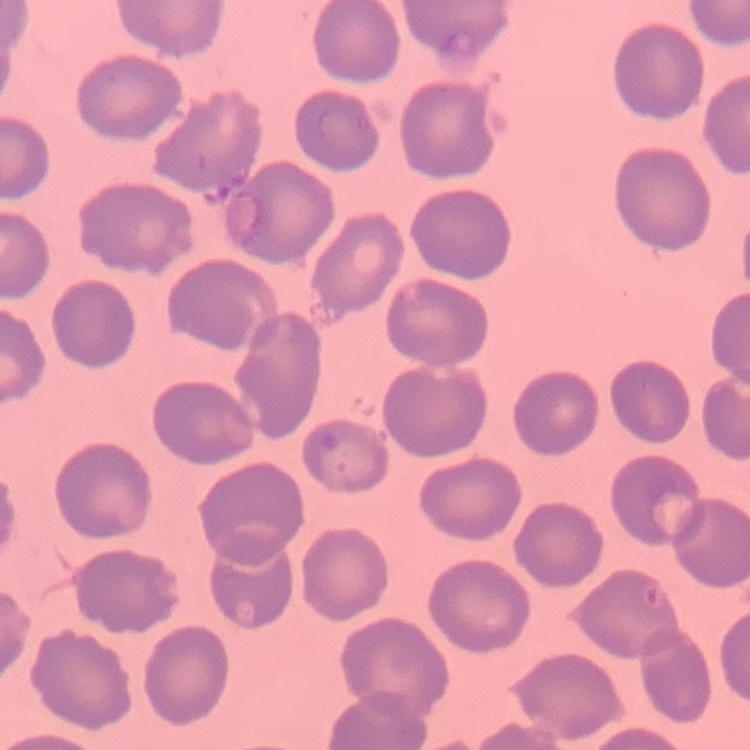 The erythrocytes exhibit no rouleaux formation. Square crop of a larger photomicrograph. Thin blood film. Field's or Giemsa stain.